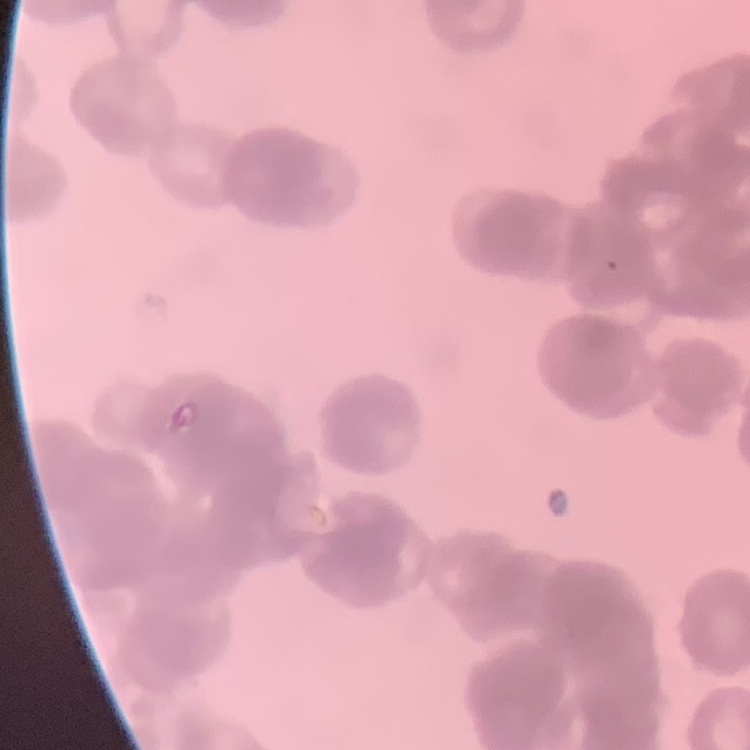
erythrocyte morphology = rouleaux formation
stain = Field's or Giemsa
preparation = thin peripheral smear
image type = square crop of a larger photomicrograph